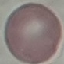
Summary:
  - Malaria status: uninfected
  - Stain: Giemsa
  - Capture: smartphone through the microscope eyepiece
  - Preparation: thin blood smear
  - Image type: automatically extracted cell patch, resized to 64 × 64 pixels